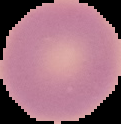
Summary:
  - Preparation: thin blood smear
  - Image type: segmented cell region with the area outside set to black
  - Image size: 121×124 pixels
  - Result: no Plasmodium parasites seen